State which parasite is depicted.
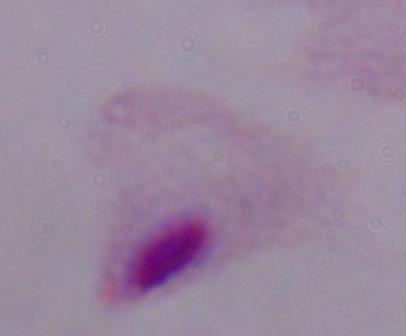
A trichomonad.

Captured at 1000x magnification. Micrograph.